Locate and identify every blood parasite.
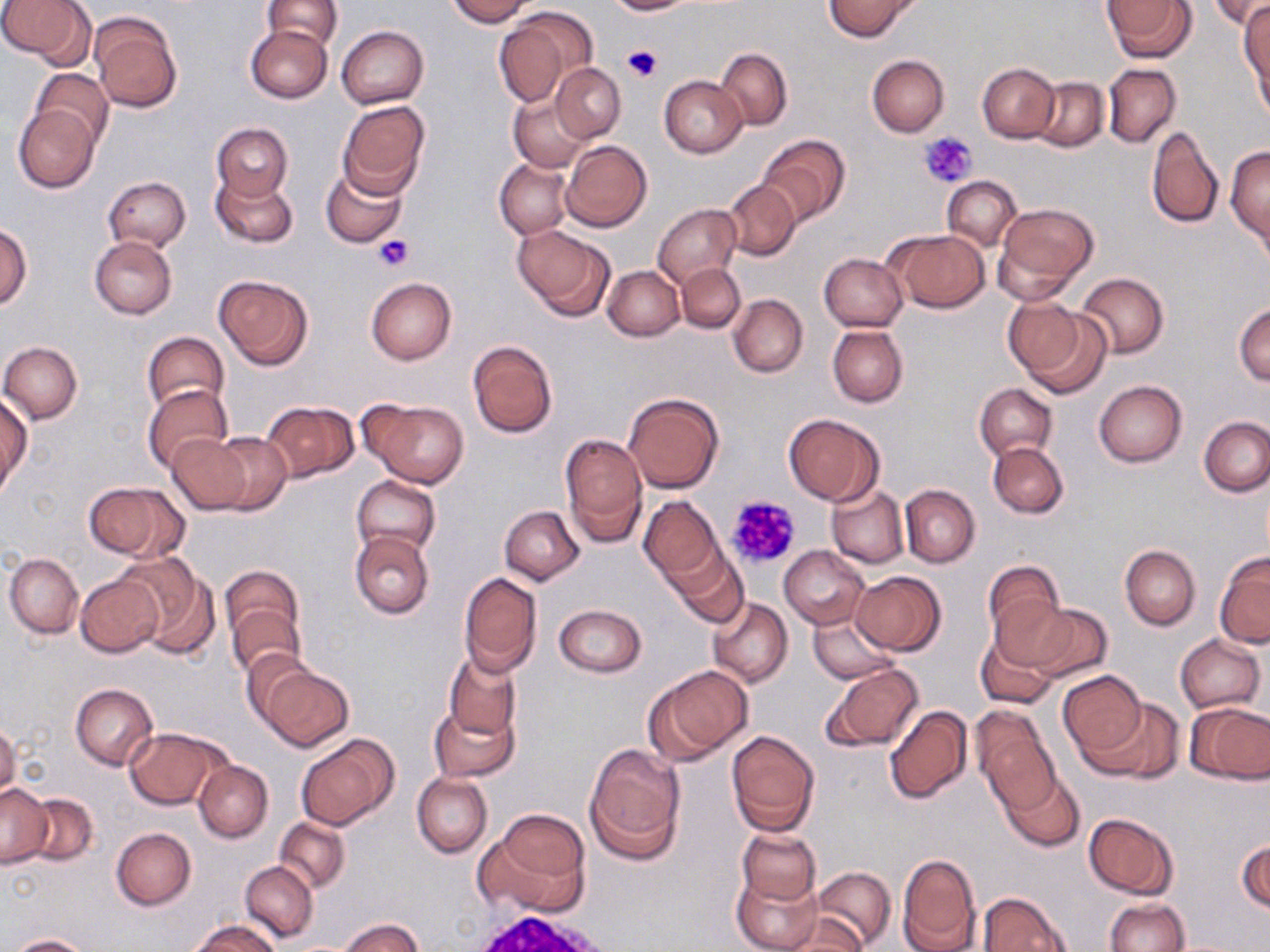

No blood parasites seen.

slide-level diagnosis = negative for blood parasites
uninfected red blood cell locations = approximate bounding boxes as [x1, y1, x2, y2] in pixels: [0, 0, 84, 61], [263, 0, 341, 52], [444, 0, 535, 26], [605, 0, 695, 15], [824, 0, 917, 41], [1103, 0, 1195, 63], [1209, 0, 1270, 30], [1240, 4, 1269, 112], [496, 6, 596, 105], [91, 13, 183, 113], [247, 23, 333, 102], [336, 25, 428, 109], [716, 48, 793, 130], [867, 55, 949, 136], [552, 63, 625, 142], [977, 63, 1060, 142], [1102, 64, 1181, 148], [31, 68, 115, 149], [659, 76, 748, 158], [1031, 76, 1108, 152], [509, 92, 591, 171], [337, 100, 431, 198], [13, 104, 101, 193], [211, 123, 293, 202], [1146, 125, 1224, 228], [756, 134, 849, 226], [562, 140, 652, 232], [1227, 145, 1270, 253], [495, 159, 573, 239], [321, 164, 408, 249], [212, 172, 298, 249], [104, 176, 190, 250], [942, 176, 1021, 250], [723, 179, 801, 261], [993, 203, 1097, 302], [652, 204, 739, 290], [0, 223, 32, 308], [512, 226, 614, 322], [887, 229, 990, 313], [88, 236, 177, 319], [818, 253, 908, 331], [677, 263, 744, 333], [603, 266, 684, 341], [1076, 272, 1169, 359], [214, 273, 312, 369], [366, 277, 456, 365], [728, 295, 808, 378], [1004, 299, 1097, 391], [1234, 303, 1270, 385], [828, 324, 908, 408], [141, 331, 229, 417], [467, 339, 558, 439], [1, 341, 82, 424], [1093, 380, 1187, 467], [975, 383, 1056, 461], [144, 384, 232, 474], [623, 392, 724, 493], [1, 396, 31, 497], [360, 399, 470, 489], [261, 401, 359, 483], [783, 413, 884, 505], [1199, 415, 1270, 496], [207, 432, 292, 516], [561, 432, 648, 543], [168, 433, 251, 513], [988, 441, 1068, 518], [352, 475, 441, 557], [84, 481, 187, 563], [826, 484, 908, 568], [900, 485, 980, 568], [639, 495, 723, 584], [500, 506, 585, 585], [350, 530, 434, 618], [1120, 544, 1200, 630], [668, 546, 749, 627], [780, 546, 869, 628], [4, 553, 82, 639], [121, 553, 216, 657], [1214, 553, 1270, 650], [982, 560, 1065, 652], [219, 565, 305, 659], [851, 571, 945, 656], [459, 572, 542, 675], [75, 573, 164, 657], [708, 597, 793, 687], [228, 603, 304, 679], [553, 604, 646, 677], [1025, 604, 1112, 684], [808, 612, 900, 683], [976, 630, 1057, 710], [1175, 634, 1265, 713], [241, 649, 317, 732], [444, 653, 521, 741], [820, 662, 923, 755], [259, 665, 353, 750], [644, 666, 752, 764], [1057, 670, 1146, 758], [71, 683, 159, 771], [1090, 696, 1184, 783], [430, 699, 518, 783], [1187, 702, 1270, 785], [883, 705, 973, 804], [973, 709, 1059, 810], [0, 720, 20, 802], [126, 726, 229, 809], [727, 729, 821, 835], [294, 736, 396, 831], [584, 745, 685, 862], [194, 759, 273, 842], [1000, 770, 1085, 851], [412, 773, 491, 857], [1, 784, 51, 867], [21, 792, 100, 866], [1084, 813, 1179, 899], [478, 816, 591, 917], [275, 817, 351, 894], [111, 827, 196, 910], [737, 828, 820, 907], [1237, 839, 1269, 916], [897, 852, 982, 952], [240, 861, 318, 942], [812, 866, 897, 950], [733, 871, 823, 952], [978, 891, 1071, 952], [1104, 899, 1189, 952], [778, 914, 867, 951], [340, 917, 422, 952], [193, 918, 280, 952], [9, 934, 93, 952]
preparation = thin blood film
image size = 1270×952 pixels
platelet locations = approximate bounding boxes as [x1, y1, x2, y2] in pixels: [623, 44, 661, 83], [921, 132, 976, 189], [374, 235, 413, 271], [727, 493, 802, 570]
field of view = single
modality = light microscopy
stain = May-Grünwald-Giemsa
magnification = 1000x